Report the malaria status of this cell.
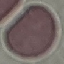
It is uninfected.

Summary:
  - Capture: smartphone through the microscope eyepiece
  - Image type: cell patch, automatically extracted from a larger field of view and resized to 64 × 64 pixels
  - Preparation: thin blood film
  - Stain: Giemsa